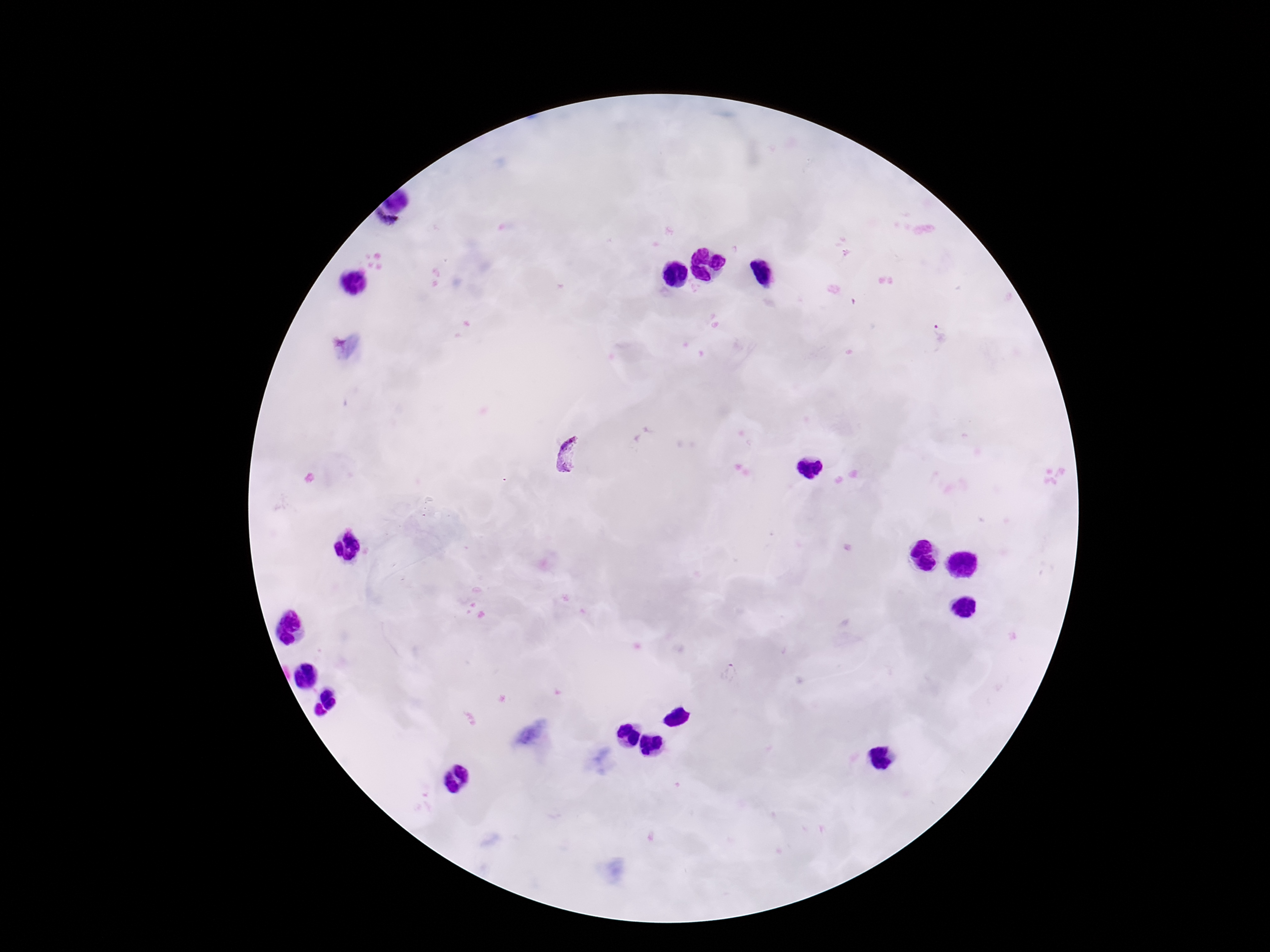
plasmodium_parasite_locations: 'approximate centers as (x, y) in pixels: (941, 333), (574, 458), (731, 673)'
image_size: 1270×952 pixels
stain: Giemsa
capture: smartphone camera through the microscope eyepiece
preparation: thick blood film
field_of_view: single
magnification: 100x
patient_malaria_status: positive